Locate every uninfected red blood cell.
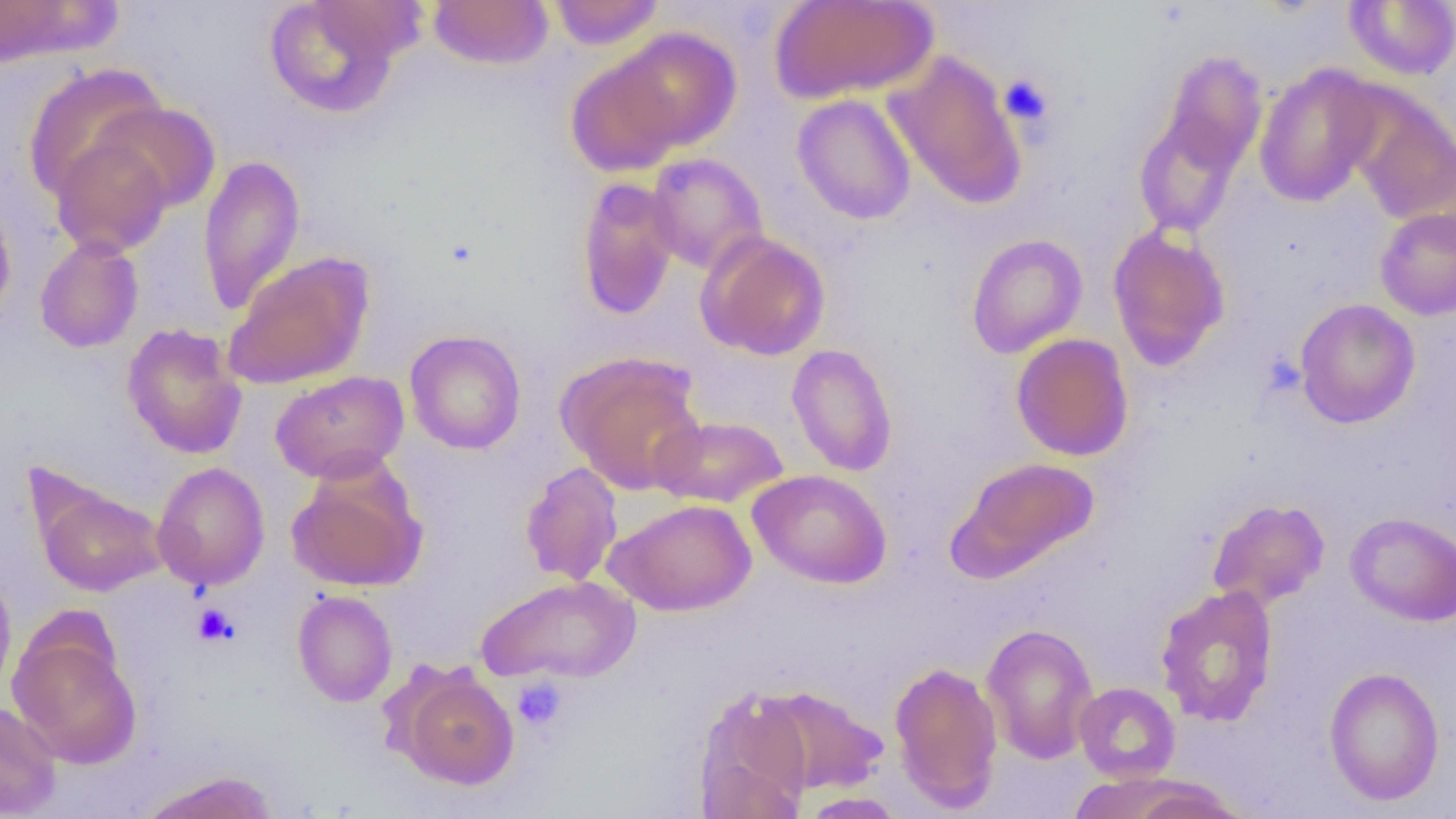

Approximate bounding boxes as named x1/y1/x2/y2 corners in pixels.
Uninfected red blood cells: (x1=0, y1=0, x2=117, y2=67), (x1=547, y1=0, x2=665, y2=50), (x1=771, y1=0, x2=937, y2=102), (x1=1343, y1=0, x2=1456, y2=80), (x1=263, y1=1, x2=404, y2=119), (x1=427, y1=1, x2=553, y2=70), (x1=610, y1=27, x2=741, y2=152), (x1=885, y1=50, x2=1027, y2=210), (x1=1157, y1=50, x2=1268, y2=176), (x1=567, y1=54, x2=685, y2=177), (x1=21, y1=64, x2=169, y2=203), (x1=1254, y1=64, x2=1382, y2=207), (x1=1344, y1=89, x2=1456, y2=226), (x1=792, y1=94, x2=916, y2=225), (x1=94, y1=101, x2=222, y2=215), (x1=1132, y1=111, x2=1246, y2=238), (x1=49, y1=134, x2=174, y2=257), (x1=646, y1=152, x2=769, y2=274), (x1=198, y1=153, x2=305, y2=316), (x1=575, y1=177, x2=681, y2=320), (x1=0, y1=195, x2=17, y2=329), (x1=1375, y1=206, x2=1456, y2=320), (x1=1107, y1=225, x2=1231, y2=370), (x1=697, y1=231, x2=831, y2=360), (x1=966, y1=233, x2=1088, y2=358), (x1=34, y1=235, x2=144, y2=353), (x1=223, y1=251, x2=374, y2=390), (x1=1294, y1=298, x2=1421, y2=428), (x1=121, y1=323, x2=248, y2=460), (x1=404, y1=329, x2=526, y2=454), (x1=1011, y1=333, x2=1134, y2=461), (x1=786, y1=343, x2=898, y2=477), (x1=557, y1=350, x2=706, y2=493), (x1=270, y1=370, x2=409, y2=483), (x1=651, y1=415, x2=789, y2=508), (x1=953, y1=456, x2=1101, y2=576), (x1=287, y1=460, x2=427, y2=593), (x1=519, y1=460, x2=624, y2=587), (x1=152, y1=461, x2=270, y2=591), (x1=749, y1=469, x2=892, y2=589), (x1=31, y1=479, x2=168, y2=597), (x1=1206, y1=498, x2=1329, y2=611), (x1=604, y1=499, x2=757, y2=616), (x1=1345, y1=512, x2=1456, y2=626), (x1=0, y1=566, x2=17, y2=698), (x1=476, y1=575, x2=640, y2=685), (x1=1155, y1=584, x2=1279, y2=727), (x1=292, y1=590, x2=397, y2=707), (x1=981, y1=622, x2=1099, y2=764), (x1=8, y1=627, x2=142, y2=769), (x1=890, y1=660, x2=1003, y2=811), (x1=1323, y1=666, x2=1445, y2=806), (x1=396, y1=668, x2=520, y2=790), (x1=1074, y1=682, x2=1180, y2=782), (x1=754, y1=685, x2=889, y2=796), (x1=693, y1=687, x2=814, y2=817), (x1=0, y1=701, x2=62, y2=817), (x1=139, y1=770, x2=280, y2=819), (x1=1114, y1=778, x2=1255, y2=819), (x1=799, y1=792, x2=906, y2=818).

Platelet locations: (x1=999, y1=73, x2=1054, y2=128), (x1=193, y1=603, x2=239, y2=647), (x1=512, y1=675, x2=568, y2=732). Slide-level diagnosis: no evidence of blood parasites. Thin blood film. Light microscopy. Single field of view. 1000x magnification. Image is 1456×819 pixels.